Comment on the morphology of the erythrocytes.
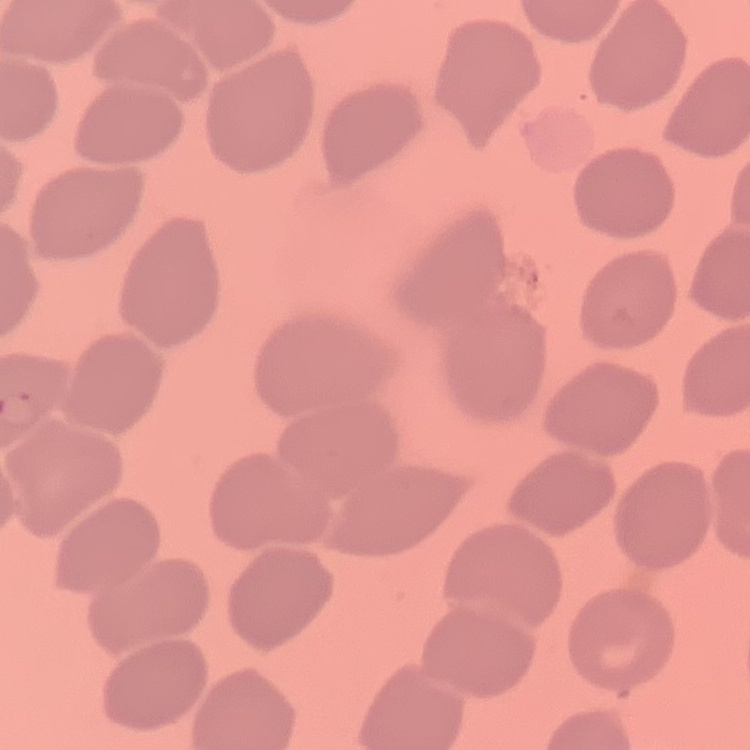
They show no rouleaux formation.

Summary:
  - Preparation: thin blood film
  - Stain: Field's or Giemsa
  - Image type: square crop of a larger photomicrograph